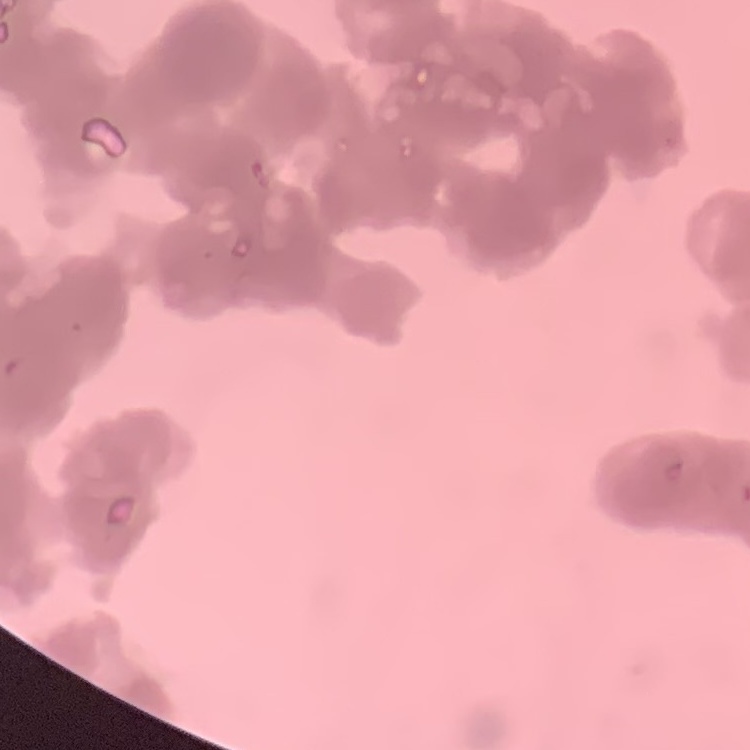
The erythrocytes show rouleaux formation. Field's or Giemsa stain. Thin blood smear. Square crop of a larger photomicrograph.